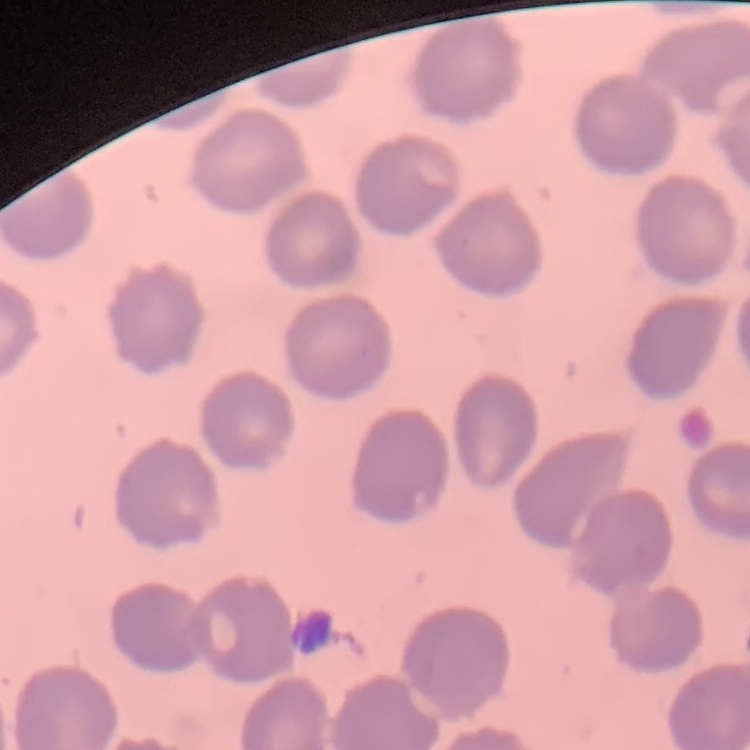
Summary:
  - Red blood cell morphology: no rouleaux formation
  - Image type: square crop of a larger photomicrograph
  - Stain: Field's or Giemsa
  - Preparation: thin blood smear